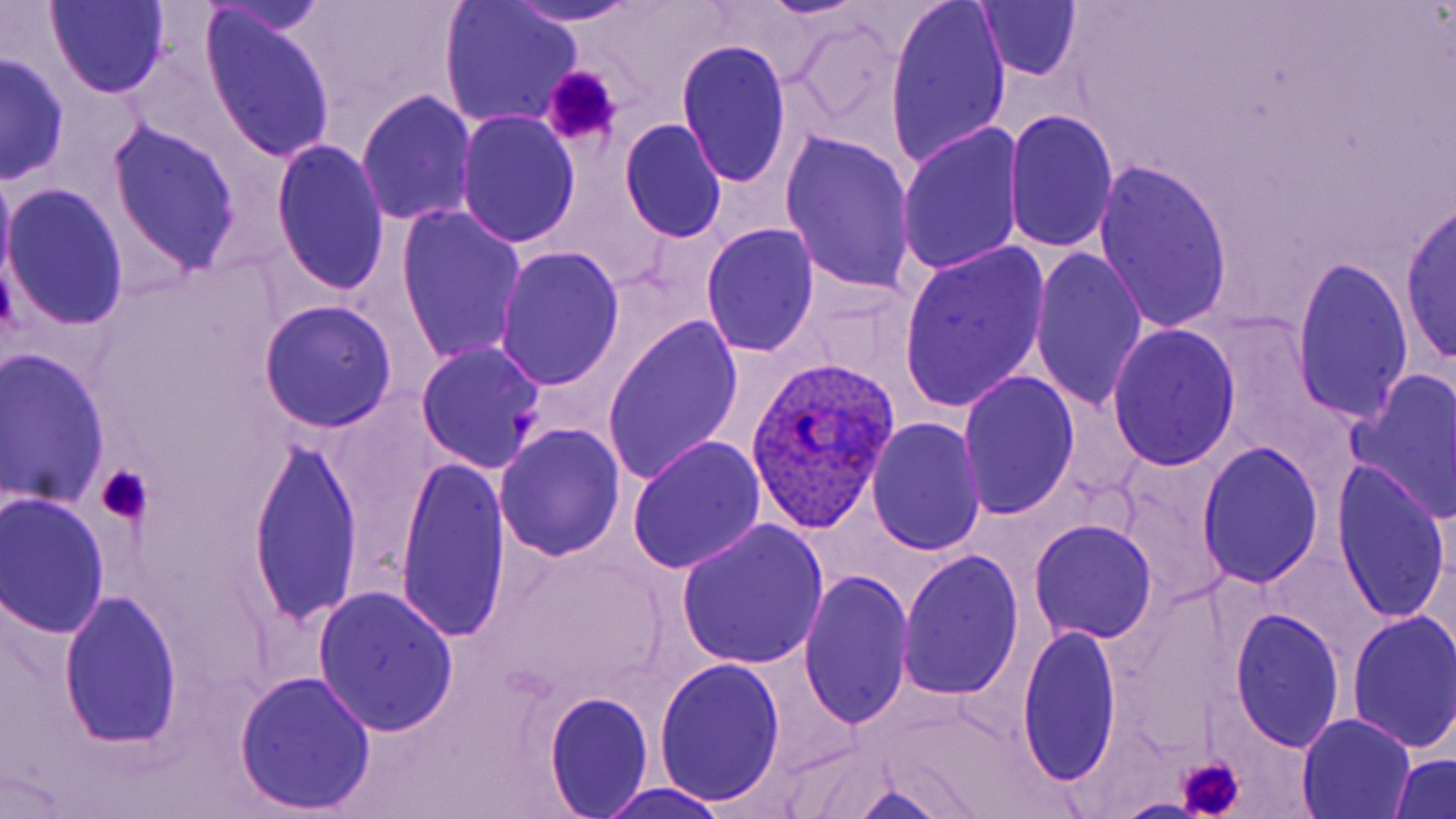 Approximate bounding boxes as named x1/y1/x2/y2 corners in pixels. Uninfected red blood cell locations: (x1=44, y1=0, x2=169, y2=99), (x1=499, y1=2, x2=652, y2=26), (x1=885, y1=2, x2=1010, y2=172), (x1=973, y1=2, x2=1084, y2=83), (x1=441, y1=3, x2=582, y2=128), (x1=199, y1=9, x2=337, y2=163), (x1=789, y1=17, x2=909, y2=143), (x1=676, y1=40, x2=792, y2=190), (x1=0, y1=54, x2=69, y2=183), (x1=358, y1=90, x2=478, y2=227), (x1=1006, y1=108, x2=1118, y2=256), (x1=457, y1=112, x2=579, y2=249), (x1=620, y1=119, x2=726, y2=242), (x1=107, y1=120, x2=243, y2=278), (x1=896, y1=124, x2=1025, y2=278), (x1=779, y1=131, x2=917, y2=299), (x1=271, y1=141, x2=391, y2=298), (x1=1093, y1=158, x2=1236, y2=337), (x1=0, y1=169, x2=15, y2=294), (x1=2, y1=185, x2=128, y2=331), (x1=1399, y1=200, x2=1455, y2=371), (x1=396, y1=205, x2=528, y2=369), (x1=701, y1=224, x2=820, y2=358), (x1=899, y1=240, x2=1051, y2=416), (x1=1029, y1=245, x2=1150, y2=412), (x1=495, y1=248, x2=625, y2=390), (x1=1290, y1=257, x2=1413, y2=427), (x1=259, y1=300, x2=396, y2=433), (x1=601, y1=315, x2=744, y2=487), (x1=1106, y1=324, x2=1241, y2=471), (x1=414, y1=341, x2=547, y2=472), (x1=0, y1=351, x2=112, y2=512), (x1=1345, y1=366, x2=1456, y2=526), (x1=959, y1=372, x2=1080, y2=519), (x1=865, y1=419, x2=987, y2=555), (x1=496, y1=423, x2=625, y2=561), (x1=246, y1=434, x2=363, y2=631), (x1=628, y1=435, x2=766, y2=575), (x1=1198, y1=442, x2=1324, y2=590), (x1=392, y1=455, x2=512, y2=646), (x1=1333, y1=462, x2=1450, y2=628), (x1=1, y1=495, x2=111, y2=638), (x1=1030, y1=519, x2=1158, y2=644), (x1=675, y1=520, x2=829, y2=671), (x1=486, y1=543, x2=669, y2=702), (x1=897, y1=550, x2=1026, y2=702), (x1=798, y1=570, x2=915, y2=732), (x1=314, y1=587, x2=459, y2=738), (x1=60, y1=591, x2=182, y2=750), (x1=1229, y1=608, x2=1347, y2=753), (x1=1346, y1=611, x2=1456, y2=754), (x1=1018, y1=621, x2=1124, y2=790), (x1=653, y1=658, x2=787, y2=809), (x1=233, y1=671, x2=378, y2=814), (x1=544, y1=693, x2=655, y2=818), (x1=1298, y1=713, x2=1415, y2=817), (x1=1388, y1=754, x2=1456, y2=819), (x1=823, y1=779, x2=966, y2=819), (x1=592, y1=782, x2=740, y2=818), (x1=1112, y1=796, x2=1211, y2=819). Plasmodium ovale-infected red blood cell locations: (x1=746, y1=355, x2=904, y2=536). Platelet locations: (x1=540, y1=66, x2=624, y2=150), (x1=95, y1=465, x2=152, y2=525), (x1=1175, y1=755, x2=1248, y2=819). Slide-level diagnosis: Plasmodium ovale. Image is 1456×819 pixels. Optical microscopy. Thin blood film. May-Grünwald-Giemsa-stained preparation. One field of a larger specimen. 1000x magnification.